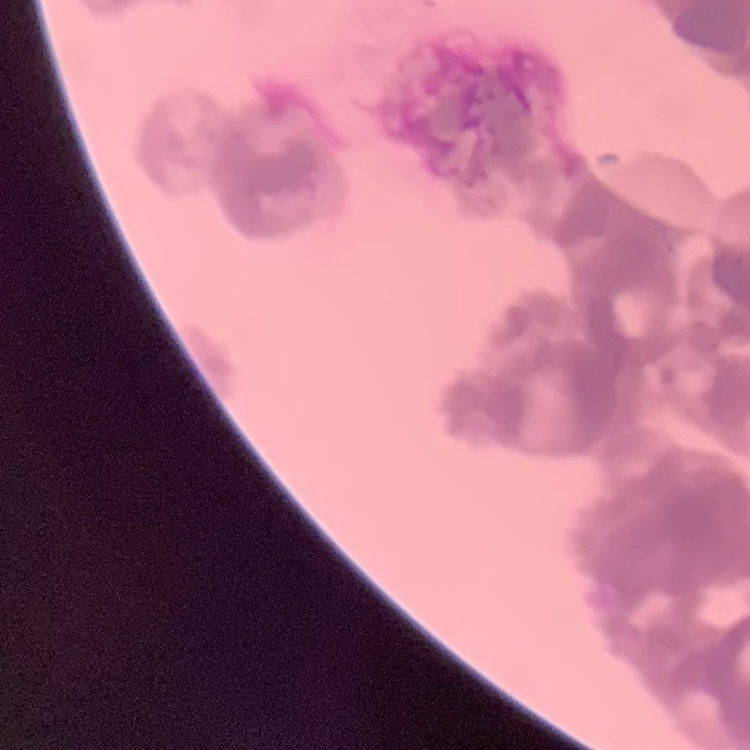 The erythrocytes show rouleaux formation. Thin blood film. One tile cut from a larger photomicrograph. Field's or Giemsa stain.